Assess the morphology of the erythrocytes.
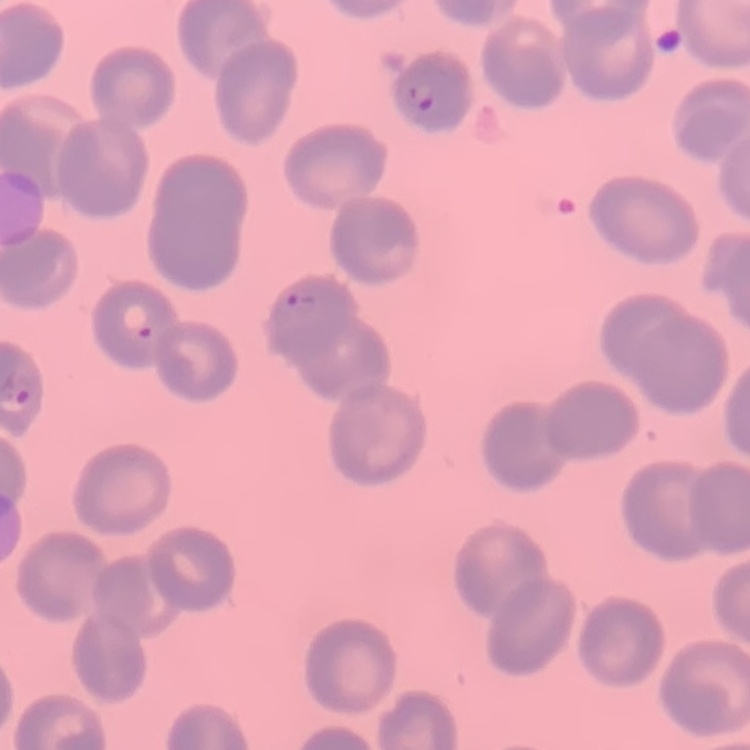

No rouleaux formation.

stain: Field's or Giemsa
preparation: thin peripheral smear
image_type: square crop of a larger photomicrograph